Assess the morphology of the red blood cells.
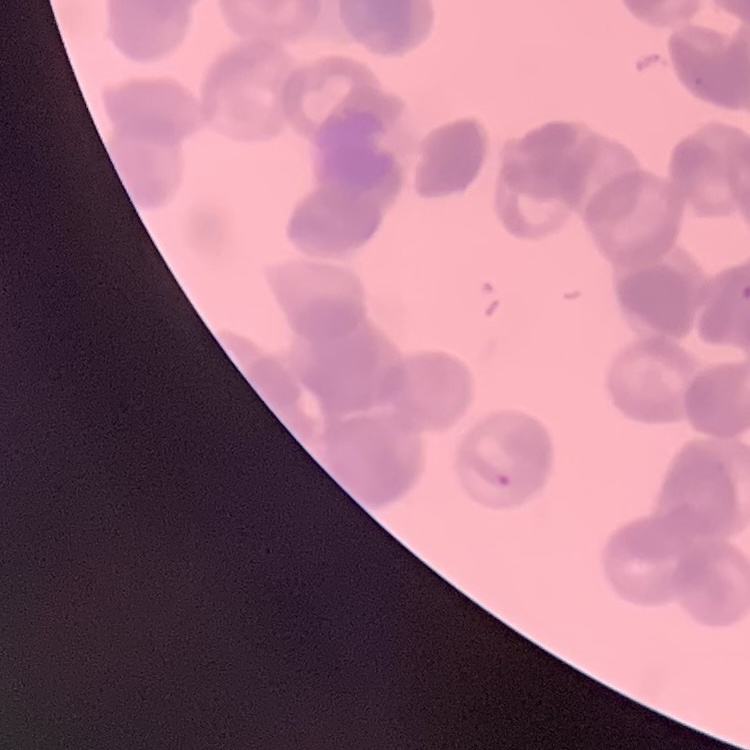

They show rouleaux formation.

preparation = thin blood smear
stain = Field's or Giemsa
image type = one tile cut from a larger photomicrograph